Assess the morphology of the erythrocytes.
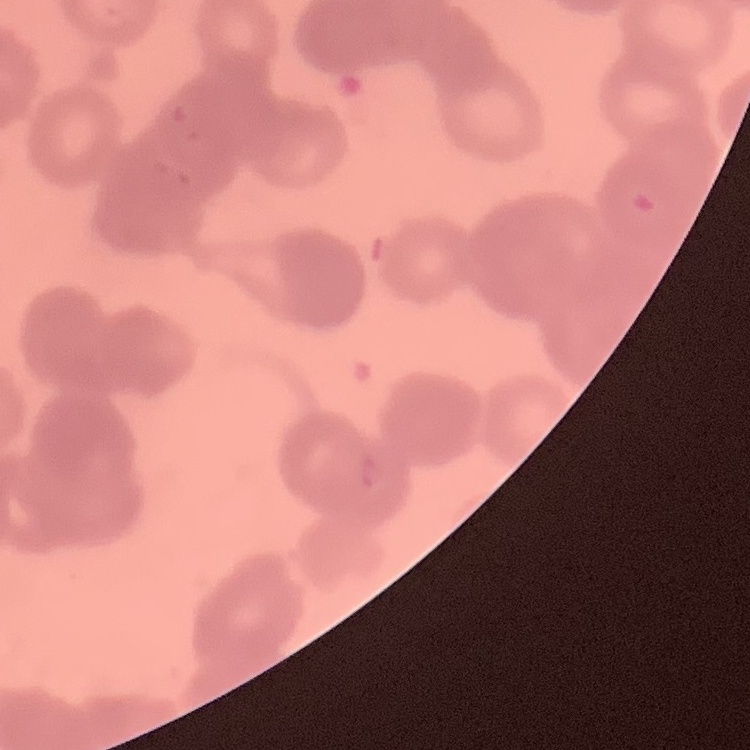
Rouleaux formation.

{
  "preparation": "thin blood film",
  "image_type": "one tile cut from a larger photomicrograph",
  "stain": "Field's or Giemsa"
}